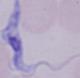

Photomicrograph. Captured at 1000x magnification. A trypanosome is shown.